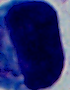

modality = micrograph
magnification = 1000x
identification = white blood cell